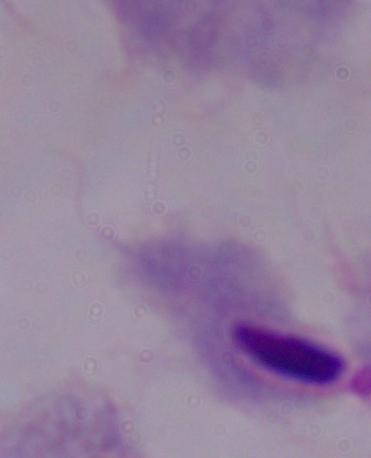
Summary:
  - Modality: photomicrograph
  - Magnification: 1000x
  - Identification: trichomonad